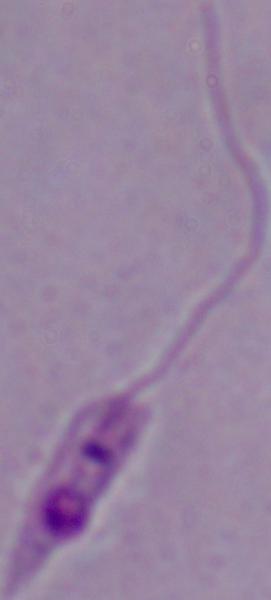

Summary:
  - Modality: micrograph
  - Identification: Leishmania
  - Magnification: 1000x